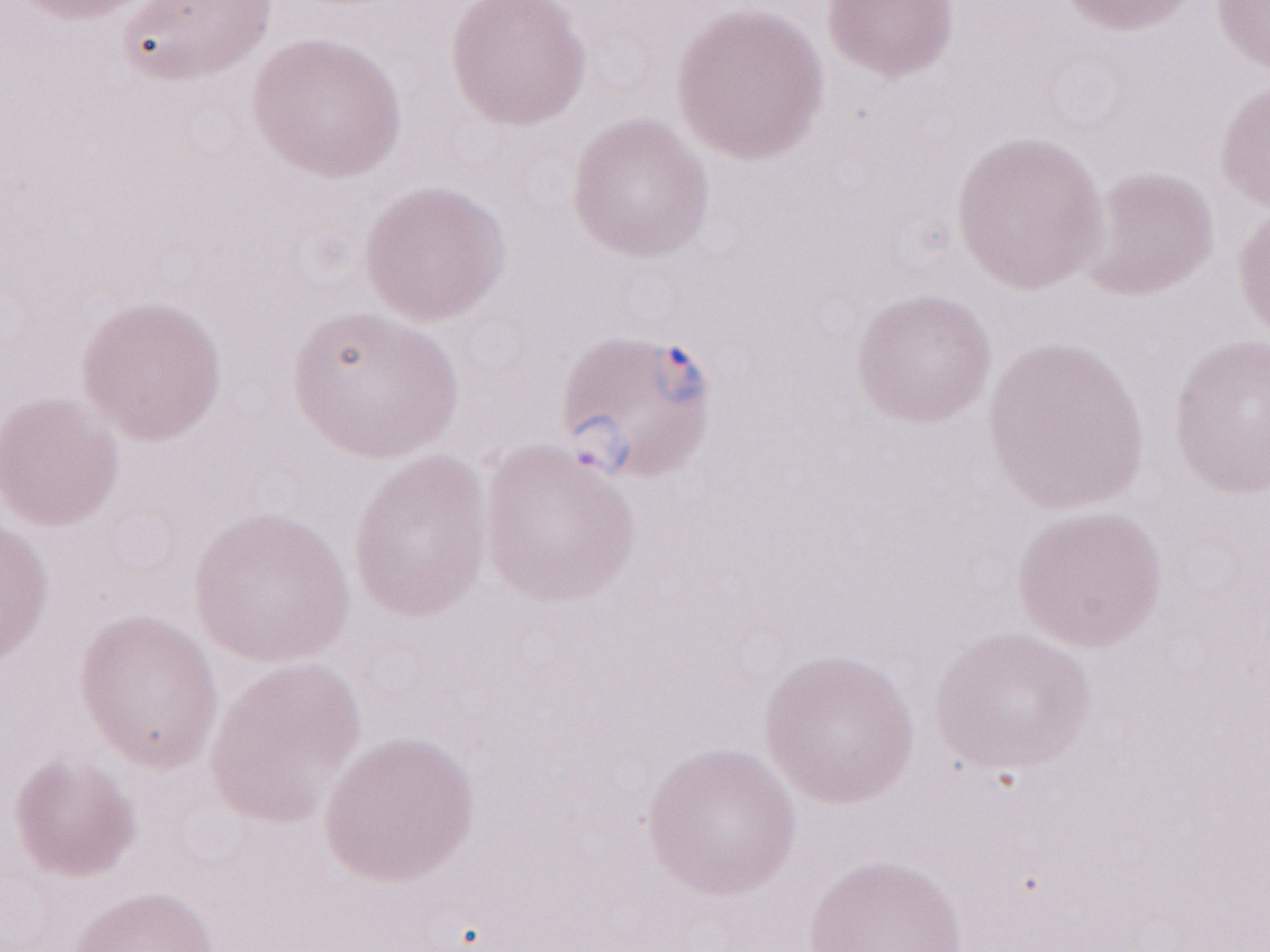

1,000x magnification. May-Grünwald-Giemsa stain. One field of this slide. Olympus BX43 microscope, Olympus DP73 camera. Image is 1270×952 pixels. Patient-level malaria diagnosis: positive. Thin blood smear.